Comment on the morphology of the red blood cells.
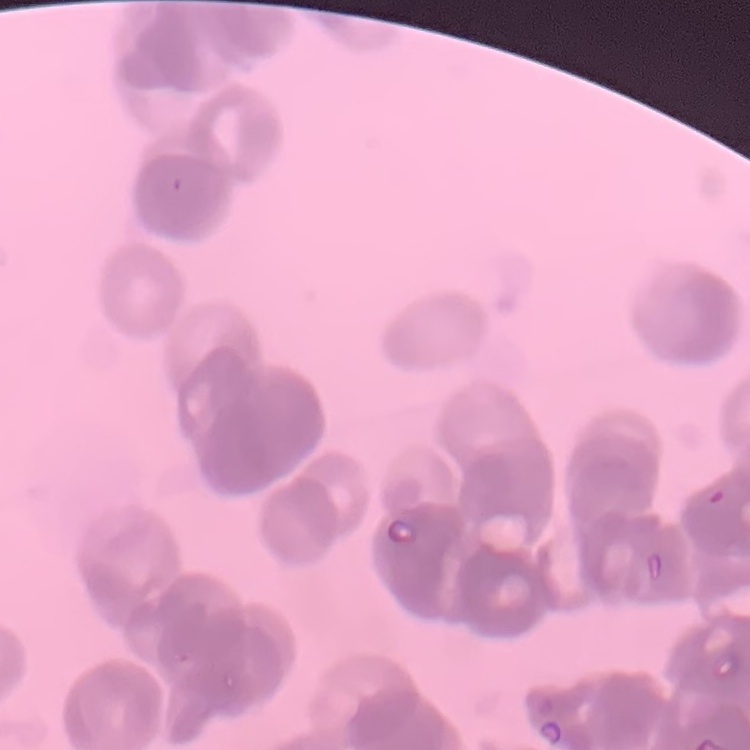

Rouleaux formation.

{
  "image_type": "square crop of a larger photomicrograph",
  "stain": "Field's or Giemsa",
  "preparation": "thin peripheral smear"
}